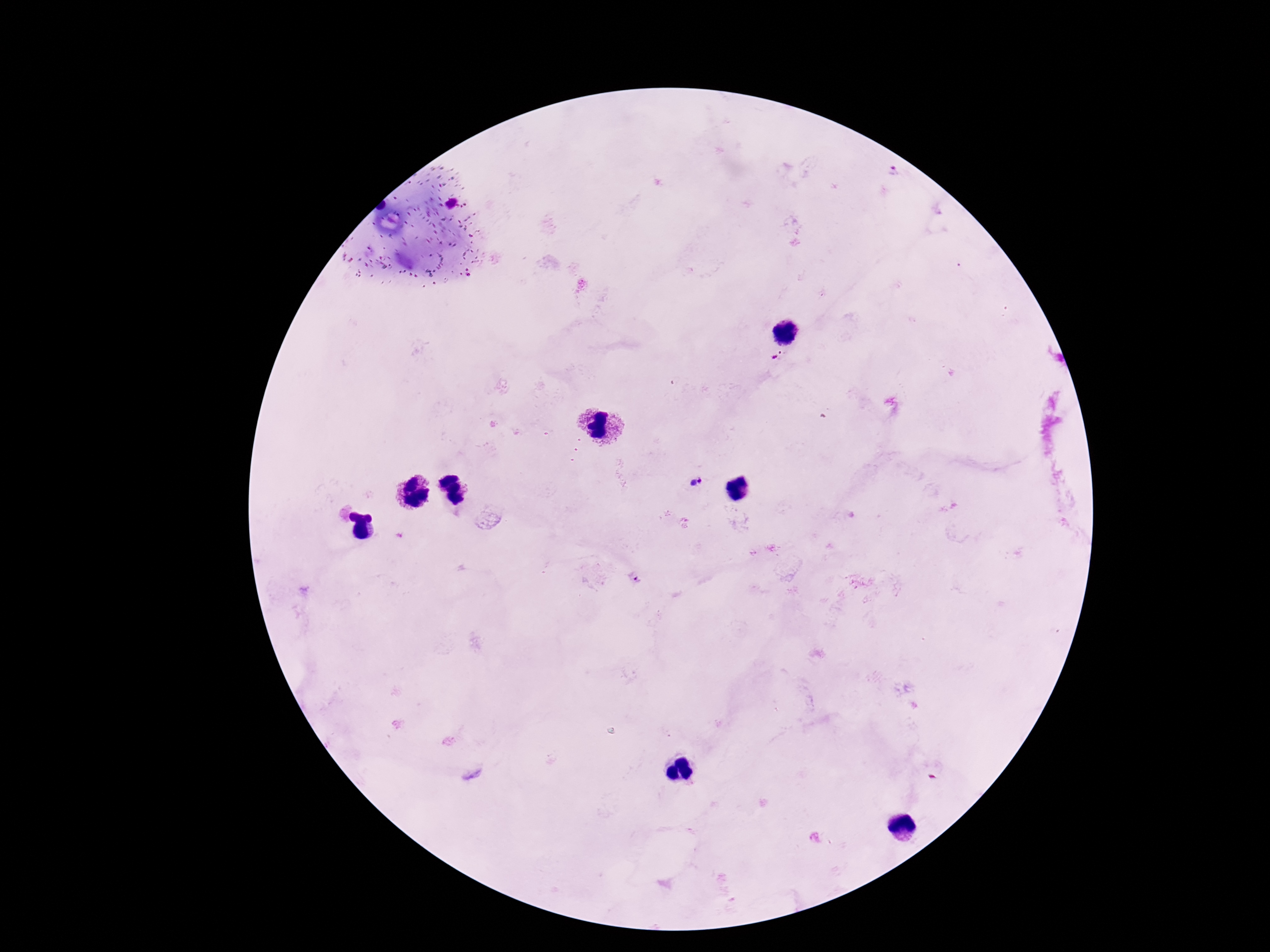
Approximate object centers, in pixels from the top-left corner.
Summary:
  - Plasmodium parasite locations: (x=894, y=173), (x=778, y=355), (x=697, y=483), (x=636, y=580)
  - Magnification: 100x
  - Field of view: one from this slide
  - Patient malaria status: positive
  - Stain: Giemsa
  - Preparation: thick peripheral-blood smear
  - Capture: smartphone camera through the microscope eyepiece
  - Image size: 1270×952 pixels